Identify the parasite.
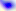
Toxoplasma gondii.

magnification = 400x
modality = photomicrograph